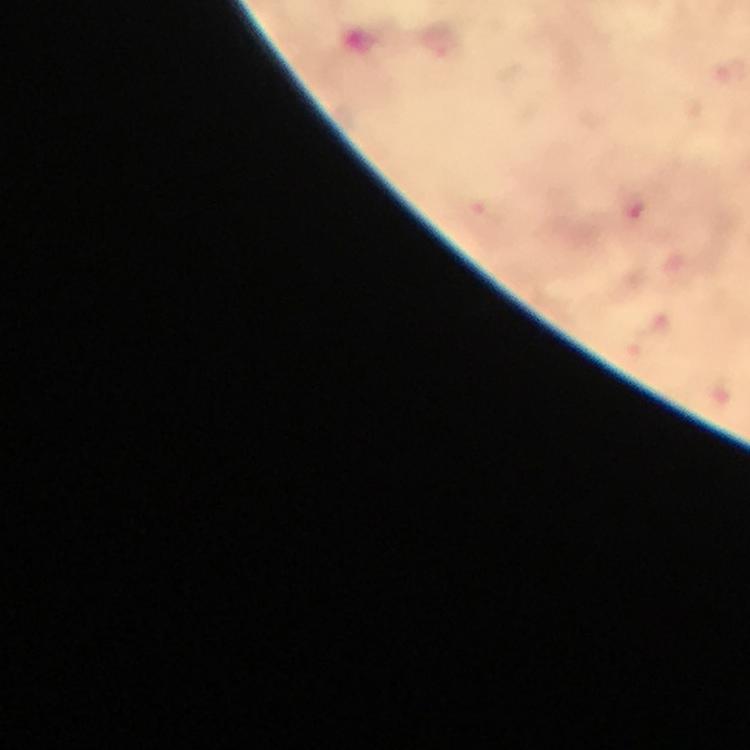
{
  "immersion_oil": "used",
  "context": "from a diagnostic examination for malaria",
  "capture": "smartphone mounted on the microscope",
  "stain": "Giemsa",
  "preparation": "thick smear",
  "malaria_parasite_locations": "approximate centers as [x, y] in pixels: [638, 213]",
  "magnification": "100x",
  "cropped_from": "one field of view",
  "image_size": "750×750 pixels"
}